Assess this cell for malaria.
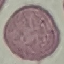
It is uninfected.

image type = automatically extracted cell patch, resized to 64 × 64 pixels
preparation = thin blood film
capture = smartphone camera at the microscope eyepiece
stain = Giemsa